Classify this cell by malaria status.
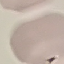

It is uninfected.

Acquired by smartphone through the microscope eyepiece. Thin blood smear. Cell patch, automatically extracted from a larger field of view and resized to 64 × 64 pixels. Giemsa-stained preparation.